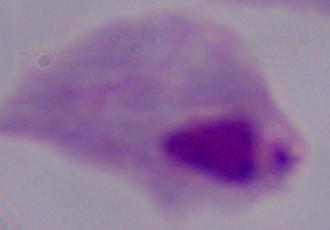 1000x magnification. A trichomonad is seen. Micrograph.